Assess this cell for malaria.
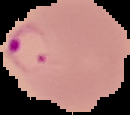
It is parasitized.

Image is 130×115 pixels. Segmented cell region on a black background. From a thin blood film.